Report the malaria status of this cell.
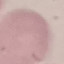

Uninfected.

Photographed with a smartphone camera at the microscope eyepiece. Giemsa stain. Cell patch, automatically extracted from a larger field of view and resized to 64 × 64 pixels. Thin blood smear.